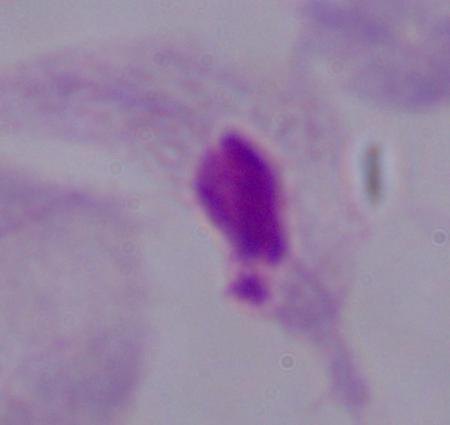
identification = trichomonad
modality = photomicrograph
magnification = 1000x